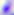
Captured at 400x magnification. Toxoplasma gondii is shown. Photomicrograph.